Look for Plasmodium parasites.
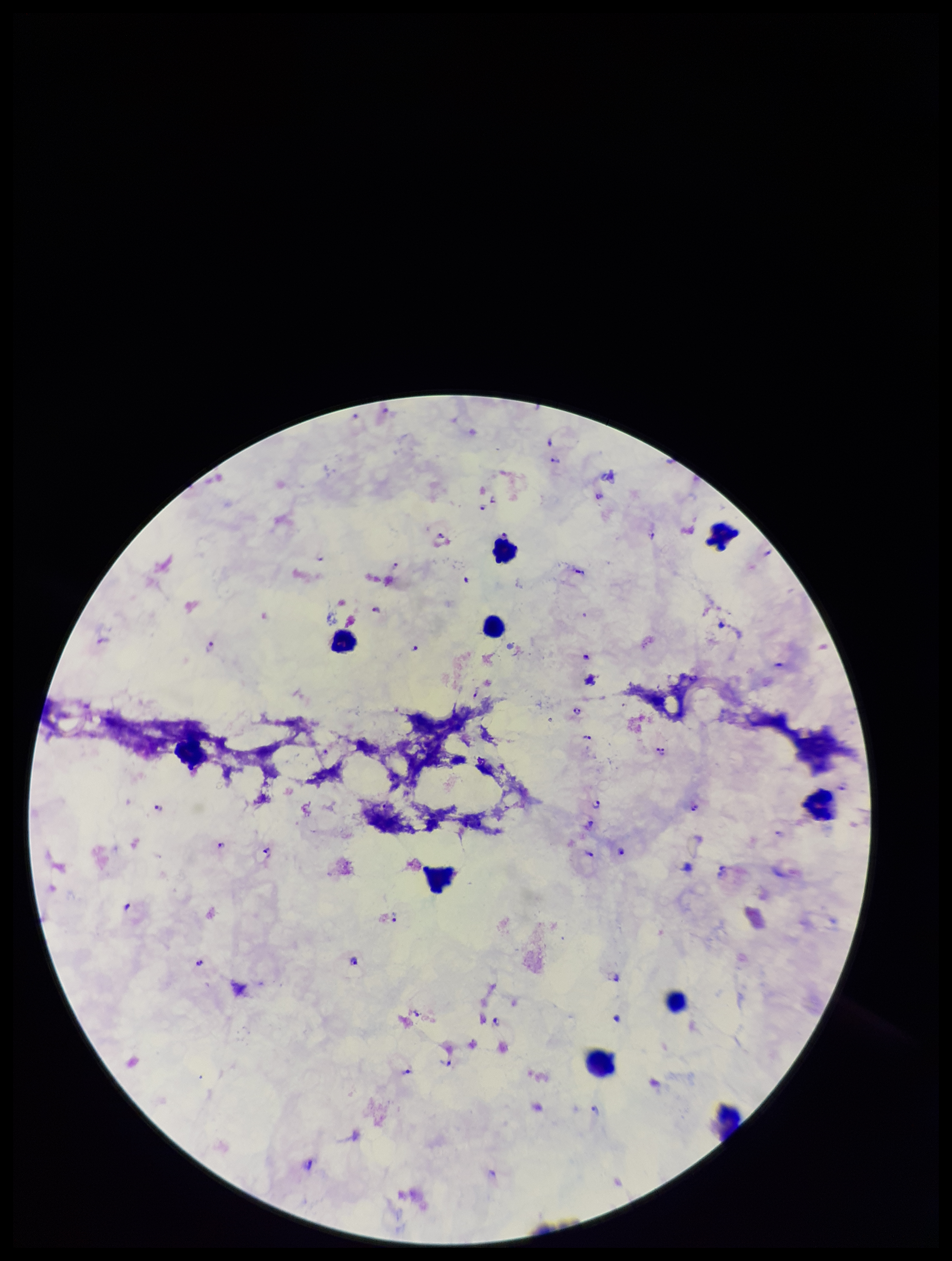
Identified.

preparation: thick
leukocyte_count: 8
stain: Giemsa
parasite_count: 29
image_size: 952×1261 pixels
patient_malaria_status: positive
capture: smartphone photograph through the microscope eyepiece
field_of_view: single
species_reported_for_this_patient: Plasmodium falciparum